Assess the morphology of the erythrocytes.
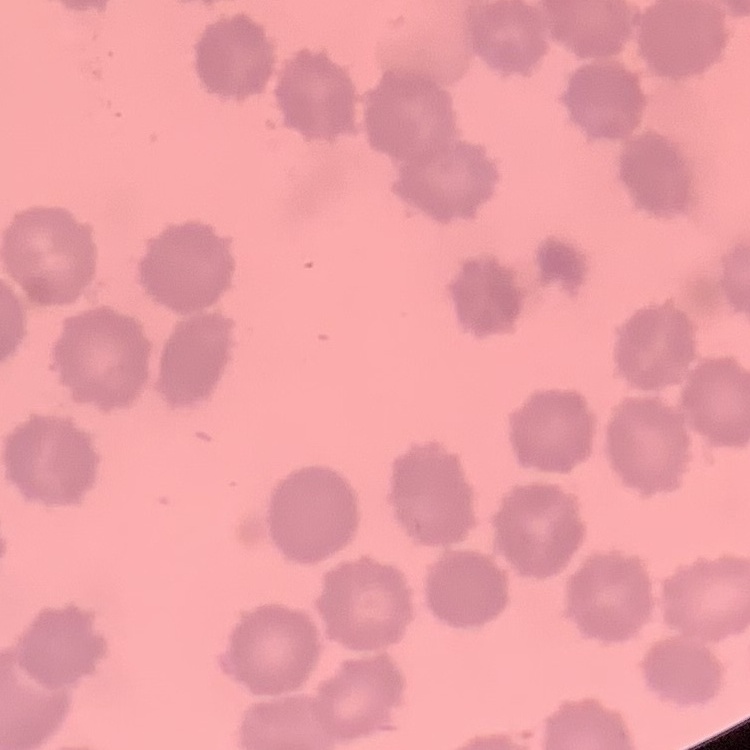
They show no rouleaux formation.

Thin blood smear. One tile cut from a larger photomicrograph. Field's or Giemsa stain.